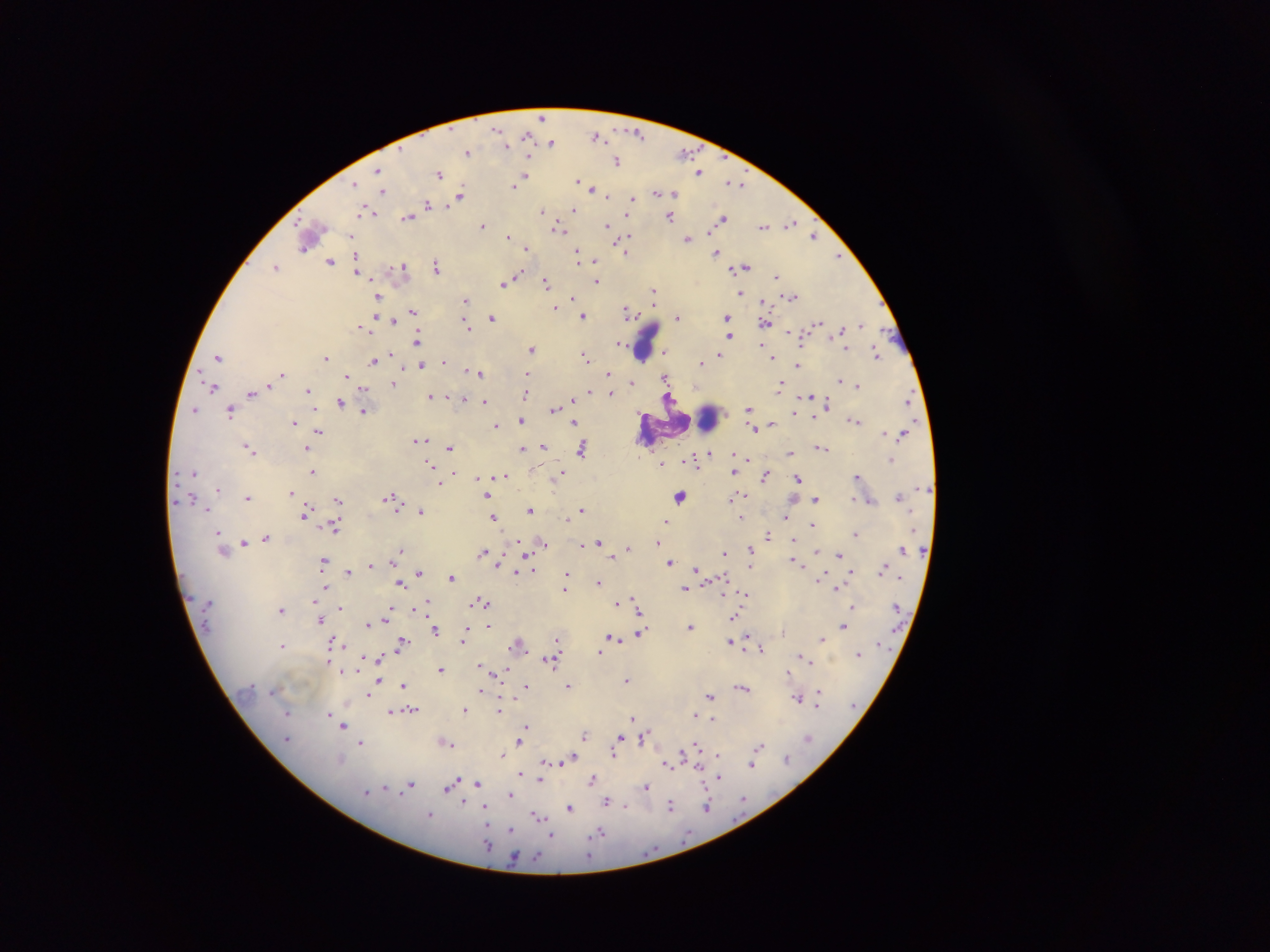

Approximate centers as x y in pixels. Leukocyte locations: 646 338; 708 418. Malaria parasite locations: 541 118; 496 129; 636 133; 597 135; 526 136; 551 143; 506 146; 467 152; 684 152; 617 162; 379 169; 699 171; 439 174; 524 177; 577 180; 732 182; 355 184; 738 184; 514 186; 592 189; 383 191; 656 192; 673 193; 607 195; 461 196; 632 199; 428 205; 574 208; 365 211; 541 211; 412 213; 670 216; 408 217; 722 219; 790 222; 483 225; 607 225; 764 226; 559 229; 629 235; 814 236; 351 237; 508 237; 687 239; 621 244; 305 248; 526 248; 626 251; 578 252; 716 253; 839 257; 595 260; 330 261; 403 265; 276 266; 745 266; 436 267; 357 271; 519 275; 777 277; 597 281; 504 283; 546 283; 654 290; 740 293; 378 296; 791 297; 573 298; 465 300; 653 302; 555 308; 412 311; 628 312; 375 315; 583 316; 677 317; 727 317; 492 318; 394 320; 765 322; 818 323; 860 325; 362 326; 468 327; 788 332; 729 336; 418 341; 619 342; 761 345; 531 349; 845 349; 664 352; 392 353; 875 354; 720 355; 218 356; 586 357; 326 358; 772 358; 373 361; 444 361; 701 362; 421 365; 797 365; 467 371; 480 373; 526 373; 609 374; 283 375; 279 376; 347 376; 664 377; 841 380; 631 382; 393 384; 858 385; 780 386; 213 387; 364 388; 308 390; 589 391; 251 393; 611 393; 525 395; 430 396; 669 396; 809 396; 908 396; 448 397; 463 400; 573 400; 484 401; 340 402; 828 403; 749 408; 195 409; 555 409; 230 411; 363 411; 814 416; 521 420; 854 420; 294 421; 574 423; 772 424; 496 425; 754 429; 319 431; 421 439; 543 446; 450 447; 821 447; 307 449; 522 449; 581 449; 250 450; 709 453; 789 454; 748 459; 892 459; 694 461; 661 464; 429 465; 193 472; 312 472; 732 472; 454 473; 560 474; 764 474; 504 476; 857 476; 479 478; 798 478; 438 482; 218 490; 291 492; 681 495; 744 495; 487 496; 899 496; 248 497; 389 497; 732 497; 853 498; 815 499; 192 500; 338 500; 393 501; 870 502; 581 509; 208 510; 421 510; 530 510; 305 512; 741 517; 787 517; 493 518; 566 518; 666 521; 812 525; 334 526; 218 533; 856 533; 768 535; 266 537; 244 542; 599 542; 657 542; 544 543; 581 544; 627 549; 903 550; 399 551; 751 551; 815 551; 484 552; 724 553; 839 555; 613 557; 793 560; 324 561; 670 563; 372 565; 749 566; 697 568; 532 570; 882 570; 852 571; 347 572; 516 572; 419 573; 567 575; 452 577; 599 582; 326 585; 401 585; 565 589; 685 589; 837 589; 746 594; 313 600; 634 600; 483 602; 616 603; 424 606; 853 607; 340 608; 391 609; 282 610; 639 610; 734 616; 386 619; 320 621; 367 624; 489 625; 690 626; 843 626; 436 631; 640 632; 464 635; 612 637; 822 638; 463 639; 557 640; 730 641; 335 643; 402 643; 518 643; 283 645; 761 648; 598 654; 858 654; 801 656; 378 658; 549 661; 806 661; 329 663; 482 665; 440 669; 343 671; 505 671; 789 671; 627 680; 377 683; 403 685; 526 685; 568 686; 743 688; 480 691; 370 693; 710 695; 818 696; 798 698; 412 710; 466 710; 500 711; 288 712; 328 713; 390 713; 696 716; 633 718; 713 719; 526 726; 342 727; 585 735; 619 736; 643 738; 287 739; 519 742; 361 743; 448 744; 695 746; 759 746; 614 753; 503 755; 718 756; 786 757; 571 758; 341 760; 565 761; 545 762; 668 764; 752 764; 698 766; 542 769; 521 774; 719 777; 593 779; 540 780; 477 784; 411 785; 385 787; 449 787; 647 787; 366 792; 510 795; 607 801; 463 803; 671 805; 625 807; 707 807; 485 808; 570 808; 430 814; 538 817; 511 830; 599 832; 550 835. One field of view. Thick blood film. Image is 1270×952 pixels. Sample from Ghana. Mobile-phone photograph taken through the microscope.